Give the extent of all Plasmodium falciparum-infected red blood cells.
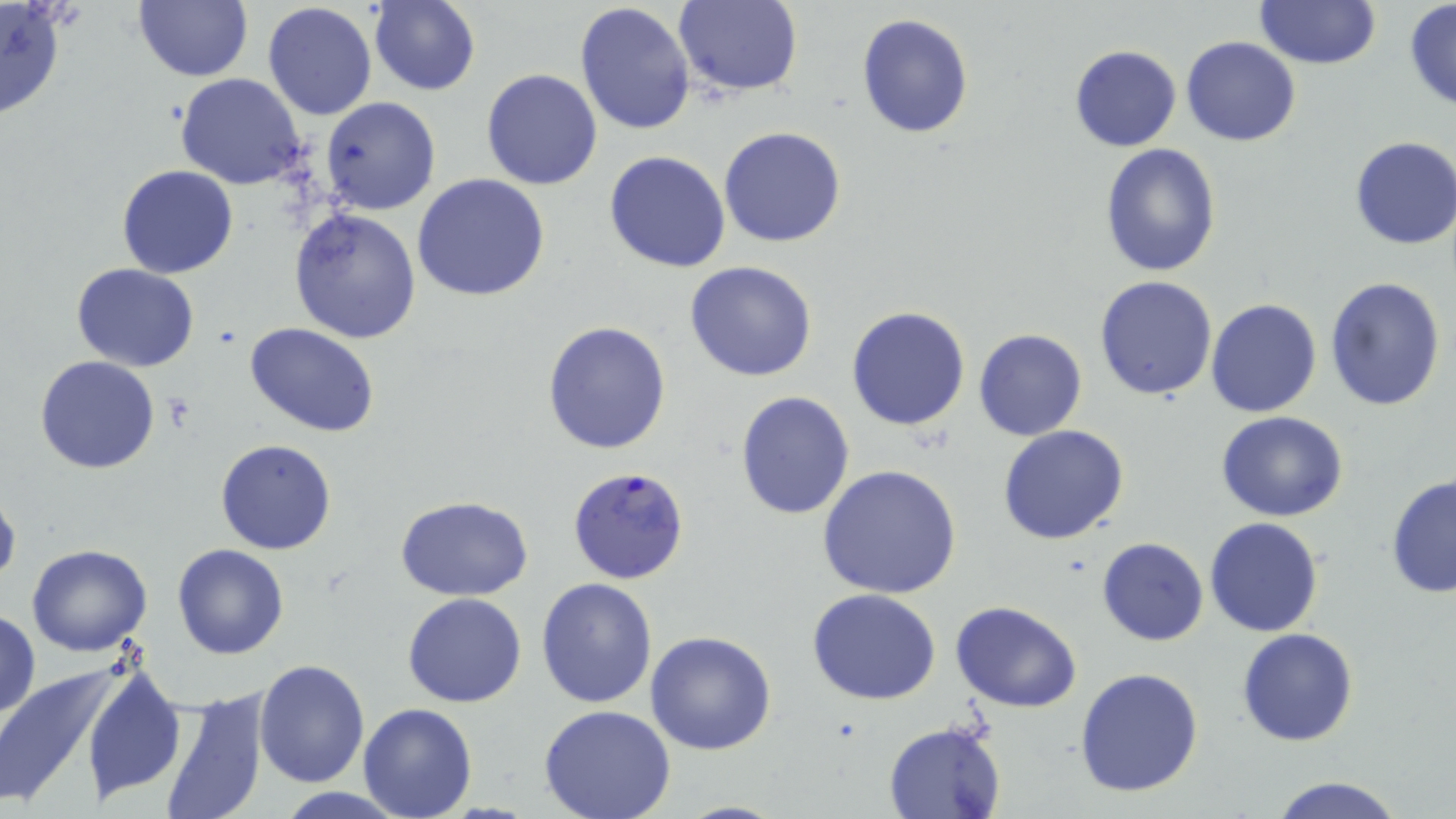

Approximate bounding boxes as [x1, y1, x2, y2] in pixels.
Plasmodium falciparum-infected red blood cells: [567, 466, 691, 585].

Uninfected red blood cell locations: [134, 0, 252, 82], [0, 1, 69, 123], [369, 1, 480, 95], [671, 1, 803, 97], [1253, 1, 1383, 70], [1404, 1, 1456, 111], [263, 2, 378, 120], [575, 2, 696, 138], [856, 13, 974, 137], [1181, 36, 1301, 146], [1068, 44, 1181, 151], [481, 69, 603, 190], [175, 74, 307, 190], [320, 96, 441, 215], [718, 126, 847, 247], [1349, 136, 1456, 250], [1099, 142, 1222, 278], [604, 151, 732, 274], [116, 165, 237, 279], [412, 172, 551, 302], [288, 207, 422, 344], [684, 261, 818, 383], [71, 263, 199, 372], [1325, 274, 1447, 411], [1095, 276, 1219, 402], [1206, 299, 1323, 418], [845, 306, 971, 431], [541, 320, 671, 454], [246, 323, 380, 437], [974, 327, 1088, 441], [36, 356, 160, 475], [735, 390, 856, 520], [1216, 411, 1349, 523], [997, 425, 1130, 546], [216, 439, 337, 555], [816, 463, 962, 599], [1384, 471, 1456, 599], [0, 485, 20, 591], [394, 496, 533, 603], [1205, 517, 1325, 637], [1097, 537, 1209, 646], [27, 544, 152, 658], [172, 544, 289, 659], [536, 577, 658, 707], [807, 587, 941, 705], [404, 593, 528, 708], [950, 602, 1083, 713], [0, 610, 40, 721], [1237, 628, 1359, 747], [646, 631, 778, 755], [81, 658, 185, 803], [255, 659, 371, 789], [0, 665, 118, 811], [1075, 667, 1204, 797], [154, 686, 271, 819], [537, 703, 677, 819], [358, 704, 479, 819], [881, 720, 1009, 819], [1264, 773, 1409, 819], [271, 788, 412, 818], [672, 800, 794, 818]. Slide-level diagnosis: Plasmodium falciparum. Thin blood film. One field of a larger specimen. May-Grünwald-Giemsa-stained preparation. Captured at 1000x magnification. Light microscopy. Image is 1456×819 pixels.